Report the malaria status.
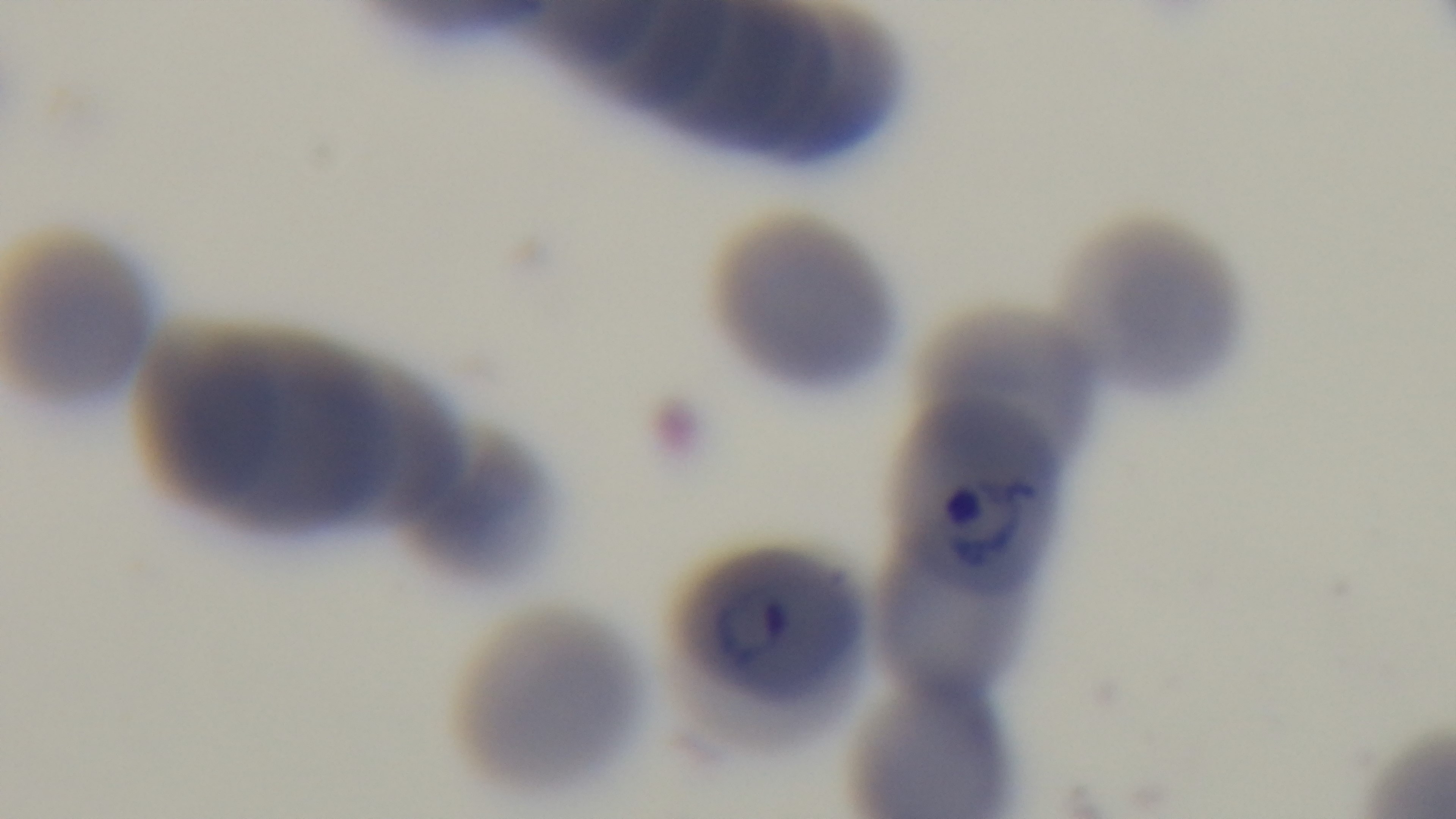
It is infected.

Photomicrograph. Single field of view. Giemsa stain. Preparation: thin blood film. 100x oil-immersion objective. Captured with a mounted 4K digital camera.